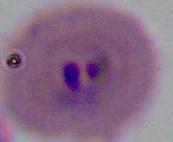
Summary:
  - Identification: Plasmodium
  - Magnification: 400x or 1000x
  - Modality: photomicrograph